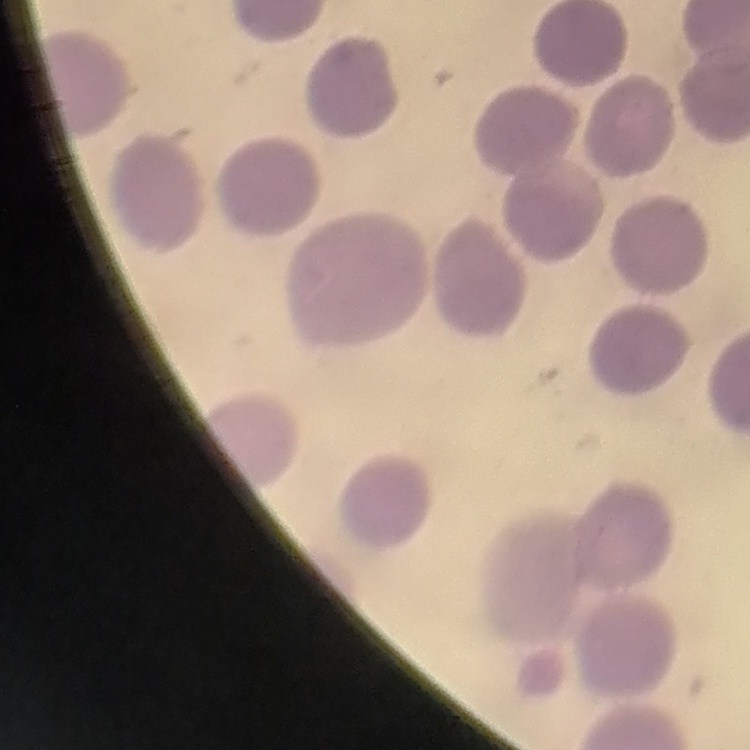
erythrocyte morphology = no rouleaux formation
stain = Field's or Giemsa
preparation = thin peripheral smear
image type = one tile cut from a larger photomicrograph